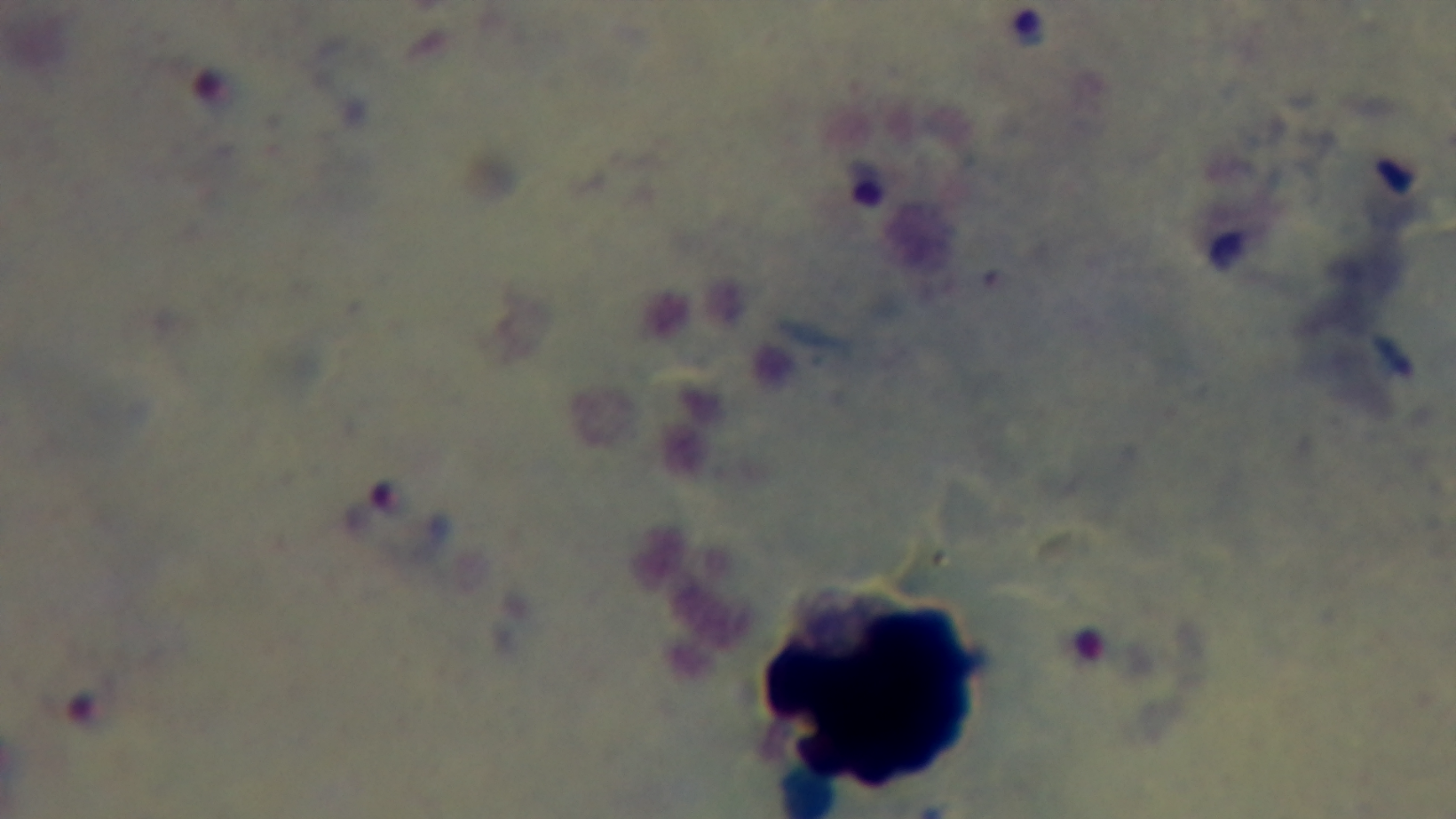
One field from the slide. Preparation: thick. Light microscopy. Captured with a mounted 4K digital camera. Oil-immersion objective, 100x. Malaria status: positive. Giemsa-stained.